Locate every blood parasite and identify its species.
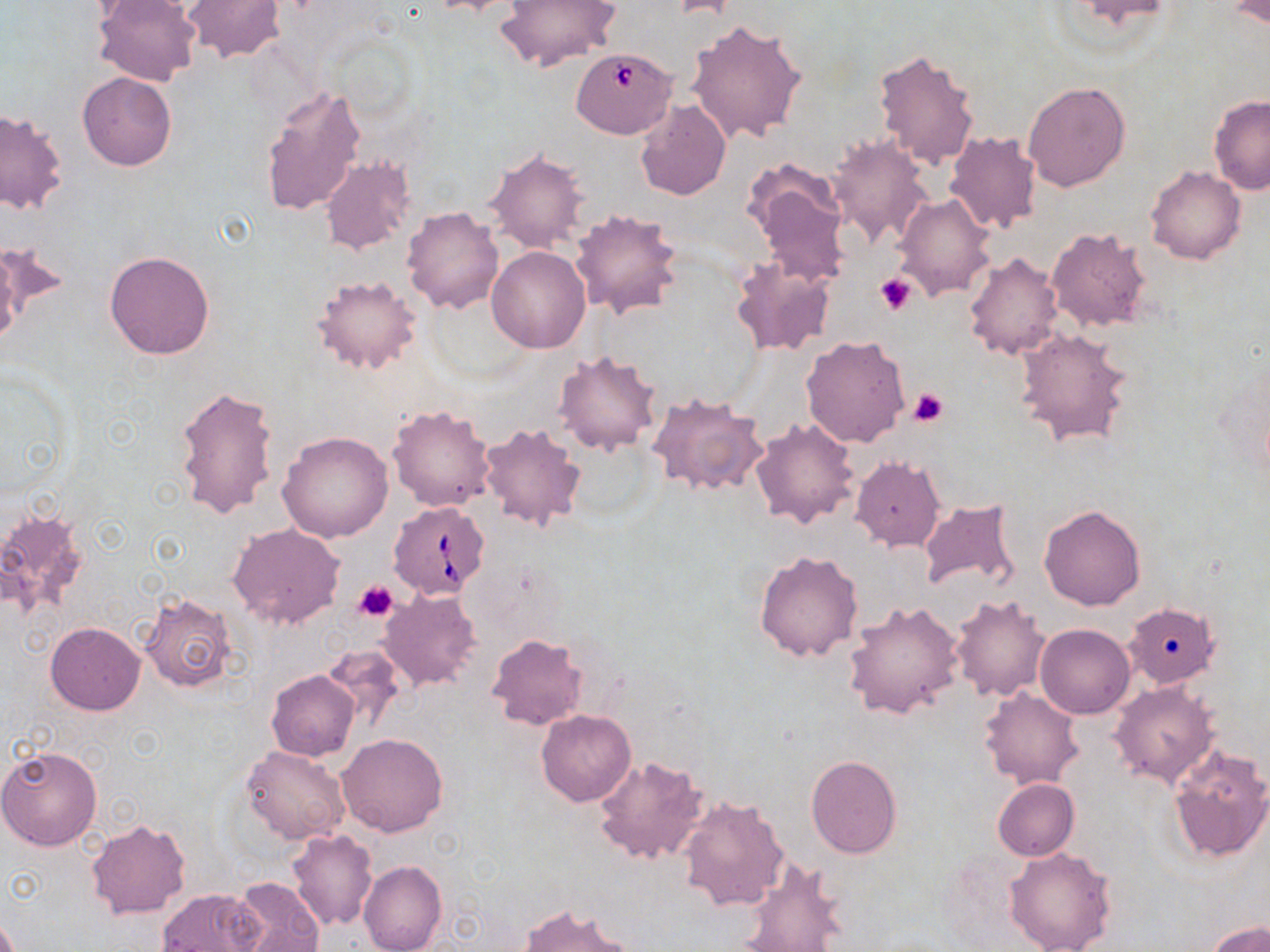
Approximate bounding boxes as (x1, y1, x2, y2) in pixels.
Babesia divergens-infected red blood cells: (575, 48, 686, 134), (389, 500, 490, 600).
No Plasmodium falciparum, Plasmodium ovale, Plasmodium malariae, Plasmodium vivax, or Trypanosoma brucei observed.

{
  "slide_level_diagnosis": "Babesia divergens",
  "modality": "optical microscopy",
  "field_of_view": "one of a larger specimen",
  "magnification": "1000x",
  "image_size": "1270×952 pixels",
  "preparation": "thin blood smear",
  "stain": "May-Grünwald-Giemsa",
  "uninfected_red_blood_cell_locations": "approximate bounding boxes as (x1, y1, x2, y2) in pixels: (91, 0, 201, 87), (181, 0, 287, 64), (419, 0, 523, 15), (497, 0, 621, 70), (1228, 1, 1269, 28), (687, 18, 808, 145), (874, 48, 980, 169), (78, 73, 177, 171), (1022, 81, 1129, 192), (258, 84, 366, 218), (1208, 95, 1270, 195), (634, 98, 732, 201), (0, 109, 66, 215), (945, 131, 1042, 236), (826, 135, 934, 249), (483, 148, 589, 252), (319, 156, 417, 255), (741, 159, 853, 288), (1145, 166, 1246, 265), (892, 193, 996, 301), (402, 206, 504, 313), (571, 208, 684, 318), (1046, 226, 1155, 333), (0, 239, 69, 334), (0, 246, 24, 349), (486, 246, 590, 352), (105, 251, 214, 359), (963, 252, 1063, 360), (730, 257, 836, 357), (311, 273, 422, 376), (1013, 327, 1132, 446), (800, 334, 911, 448), (554, 350, 663, 457), (175, 385, 280, 520), (647, 392, 767, 498), (386, 403, 495, 512), (750, 417, 860, 529), (479, 422, 586, 532), (278, 431, 394, 542), (851, 457, 945, 551), (917, 497, 1023, 595), (1038, 504, 1146, 611), (0, 509, 92, 619), (228, 523, 345, 630), (754, 550, 863, 661), (377, 589, 482, 691), (950, 592, 1050, 703), (139, 593, 238, 693), (1123, 594, 1220, 690), (843, 599, 962, 720), (45, 622, 146, 715), (1036, 624, 1135, 719), (486, 632, 590, 731), (320, 642, 407, 731), (267, 670, 360, 760), (1109, 681, 1219, 788), (979, 687, 1084, 790), (536, 710, 637, 806), (338, 734, 446, 837), (0, 744, 103, 852), (1165, 744, 1270, 864), (241, 745, 351, 847), (805, 754, 901, 858), (594, 755, 710, 866), (272, 774, 376, 902), (993, 779, 1079, 861), (677, 794, 791, 911), (85, 817, 189, 920), (287, 830, 378, 930), (1004, 847, 1116, 952), (738, 858, 849, 951), (358, 860, 446, 952), (231, 875, 323, 952), (157, 888, 265, 952), (519, 903, 637, 952), (1208, 921, 1270, 952)",
  "platelet_locations": "approximate bounding boxes as (x1, y1, x2, y2) in pixels: (875, 274, 916, 315), (909, 388, 949, 427), (354, 579, 398, 621)"
}